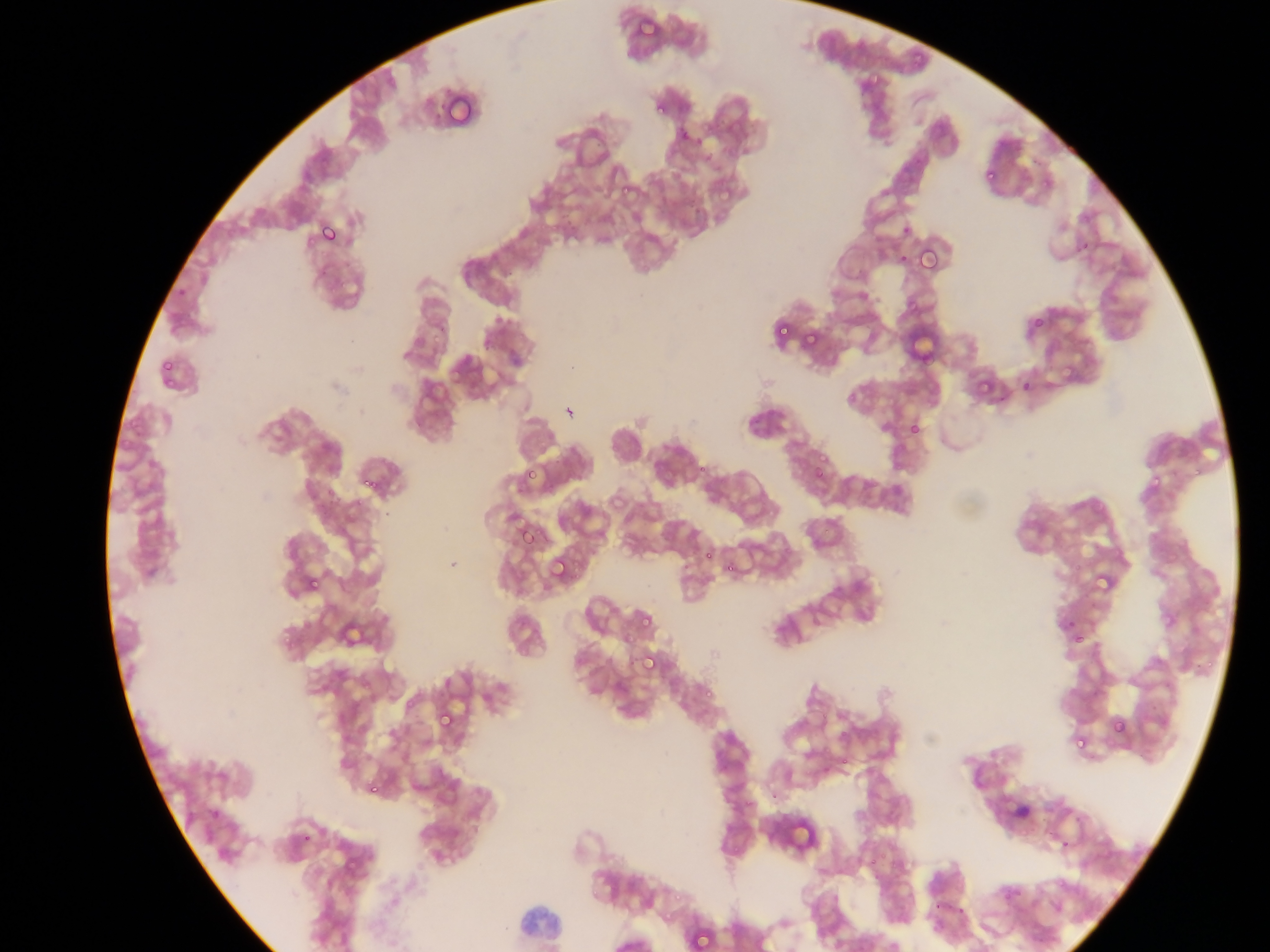
preparation: thin blood smear
image_size: 1270×952 pixels
leukocyte_locations: 'approximate bounding boxes as {left, top, right, bottom} in pixels: {514, 902, 571, 952}'
field_of_view: single
plasmodium_parasite_locations: 'approximate bounding boxes as {left, top, right, bottom} in pixels (subset; some below the resolvable size): {869, 75, 877, 83}, {656, 107, 666, 115}, {987, 169, 997, 180}, {1043, 181, 1050, 190}, {621, 186, 631, 193}, {318, 225, 339, 244}, {1082, 244, 1092, 250}, {918, 249, 938, 271}, {899, 254, 907, 262}, {178, 287, 187, 295}, {1033, 319, 1042, 327}, {779, 325, 792, 335}, {434, 334, 439, 342}, {162, 361, 174, 370}, {164, 378, 175, 388}, {1022, 381, 1028, 392}, {912, 422, 919, 433}, {819, 455, 828, 461}, {698, 466, 709, 474}, {528, 468, 538, 481}, {1194, 469, 1201, 477}, {815, 471, 824, 479}, {1150, 475, 1161, 488}, {364, 479, 373, 490}, {327, 490, 338, 495}, {521, 529, 534, 545}, {705, 550, 714, 558}, {1073, 563, 1081, 571}, {570, 564, 582, 574}, {727, 564, 735, 572}, {294, 567, 302, 573}, {572, 574, 581, 580}, {311, 578, 319, 588}, {642, 617, 651, 626}, {1068, 619, 1074, 627}, {286, 633, 298, 646}, {625, 633, 635, 641}, {1075, 634, 1087, 642}, {285, 636, 290, 644}, {641, 659, 656, 669}, {1205, 661, 1214, 669}, {705, 691, 713, 697}, {406, 699, 417, 708}, {440, 713, 453, 726}, {1113, 722, 1128, 737}, {1075, 739, 1085, 747}, {841, 757, 849, 766}, {370, 785, 376, 794}, {746, 799, 751, 807}, {210, 812, 221, 820}, {303, 834, 310, 842}, {733, 843, 742, 854}, {880, 847, 887, 859}, {870, 854, 877, 867}, {592, 889, 599, 898}, {675, 893, 682, 901}, {934, 902, 940, 911}, {958, 909, 966, 916}, {696, 932, 710, 948} | approximate {x, y} pixel centers of objects too small to bound: {449, 91}, {443, 106}, {684, 137}, {699, 142}, {905, 230}, {336, 499}, {359, 503}, {1065, 842}, {667, 916}'
capture: mobile-phone photograph through a microscope
country: Ghana